Classify this cell by malaria status.
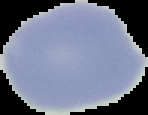

It is uninfected.

From a thin blood film. Image is 148×115 pixels. Segmented cell region on a black background.